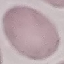
Summary:
  - Result: negative for malaria parasites
  - Stain: Giemsa
  - Capture: smartphone camera at the microscope eyepiece
  - Image type: automatically extracted cell patch, resized to 64 × 64 pixels
  - Preparation: thin smear